Describe the morphology of the erythrocytes.
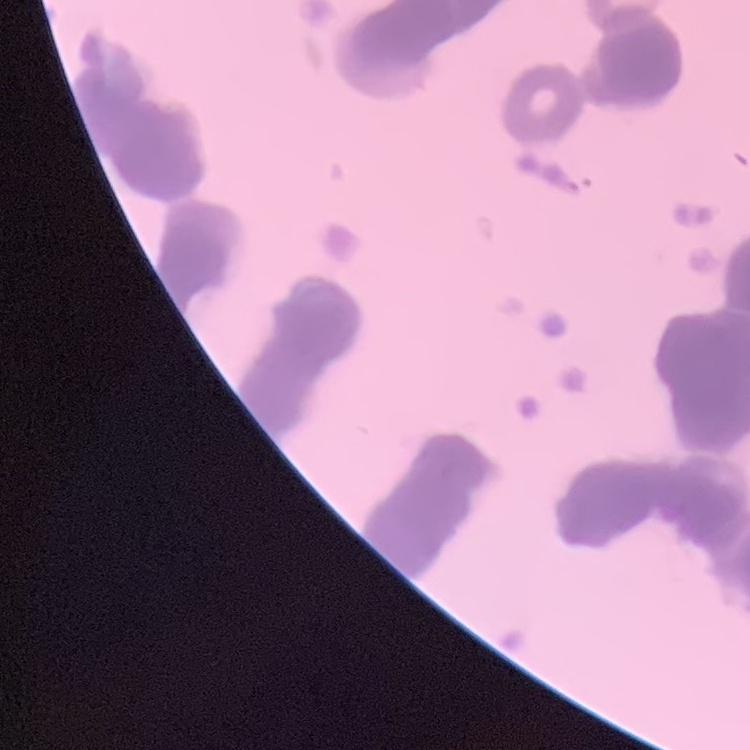
They show rouleaux formation.

stain = Field's or Giemsa
preparation = thin blood smear
image type = square crop of a larger photomicrograph